Give the preparation type.
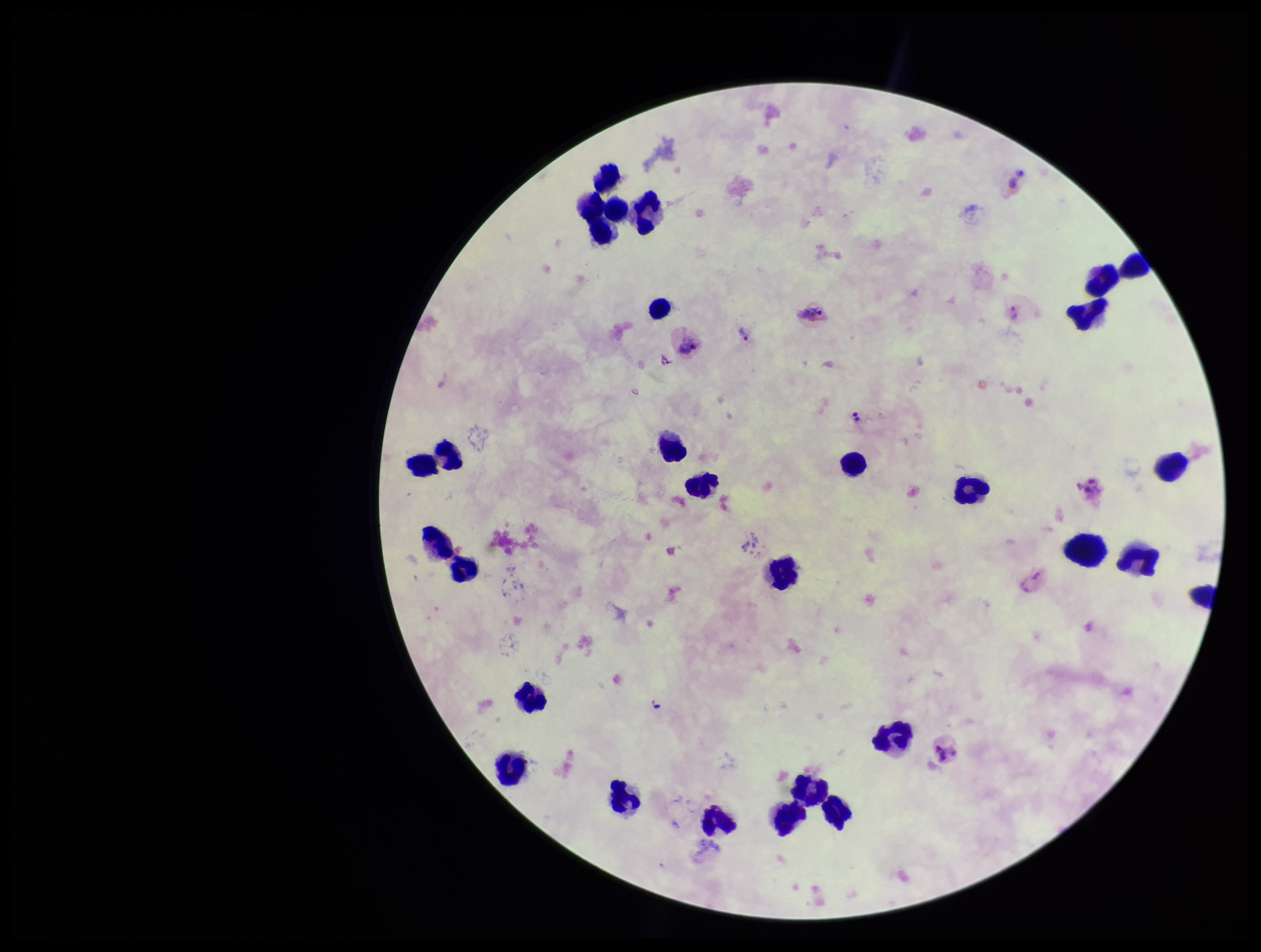
A thick smear.

Summary:
  - Image size: 1261×952 pixels
  - Plasmodium parasites: detected
  - Field of view: one from this slide
  - Stain: Giemsa
  - Species reported for this patient: Plasmodium vivax
  - Parasite count: 4
  - Capture: smartphone photograph through the microscope eyepiece
  - Leukocyte count: 29
  - Patient malaria status: infected